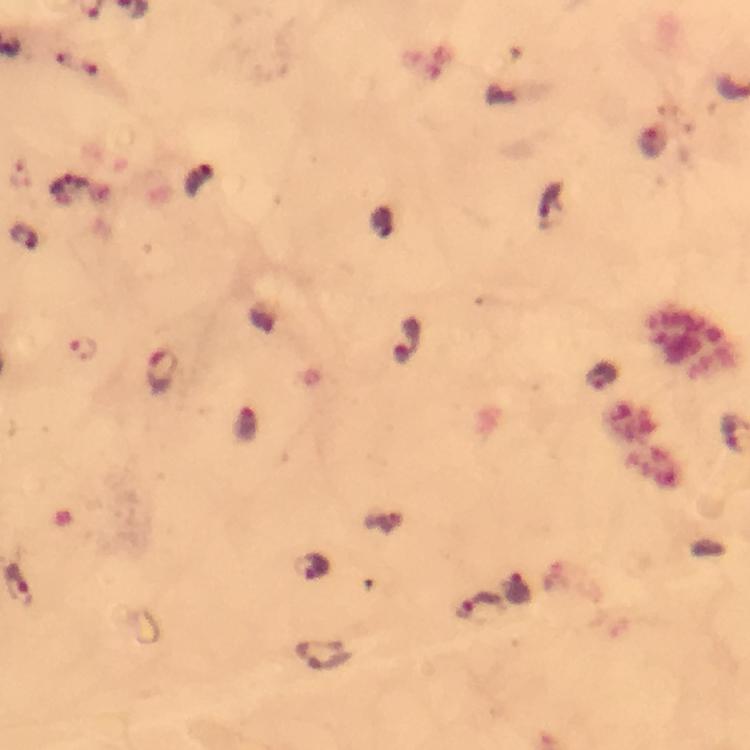

Approximate centers as [x, y] in pixels.
Summary:
  - Plasmodium parasite locations: [409, 338], [83, 348], [163, 370], [601, 378], [313, 564], [17, 584], [518, 589], [480, 608], [323, 655]
  - Image size: 750×750 pixels
  - Immersion oil: applied
  - Stain: Giemsa
  - Cropped from: a single field of view
  - Context: from a diagnostic examination for malaria
  - Capture: smartphone mounted on the microscope
  - Preparation: thick blood film
  - Magnification: 100x